Locate every Plasmodium parasite.
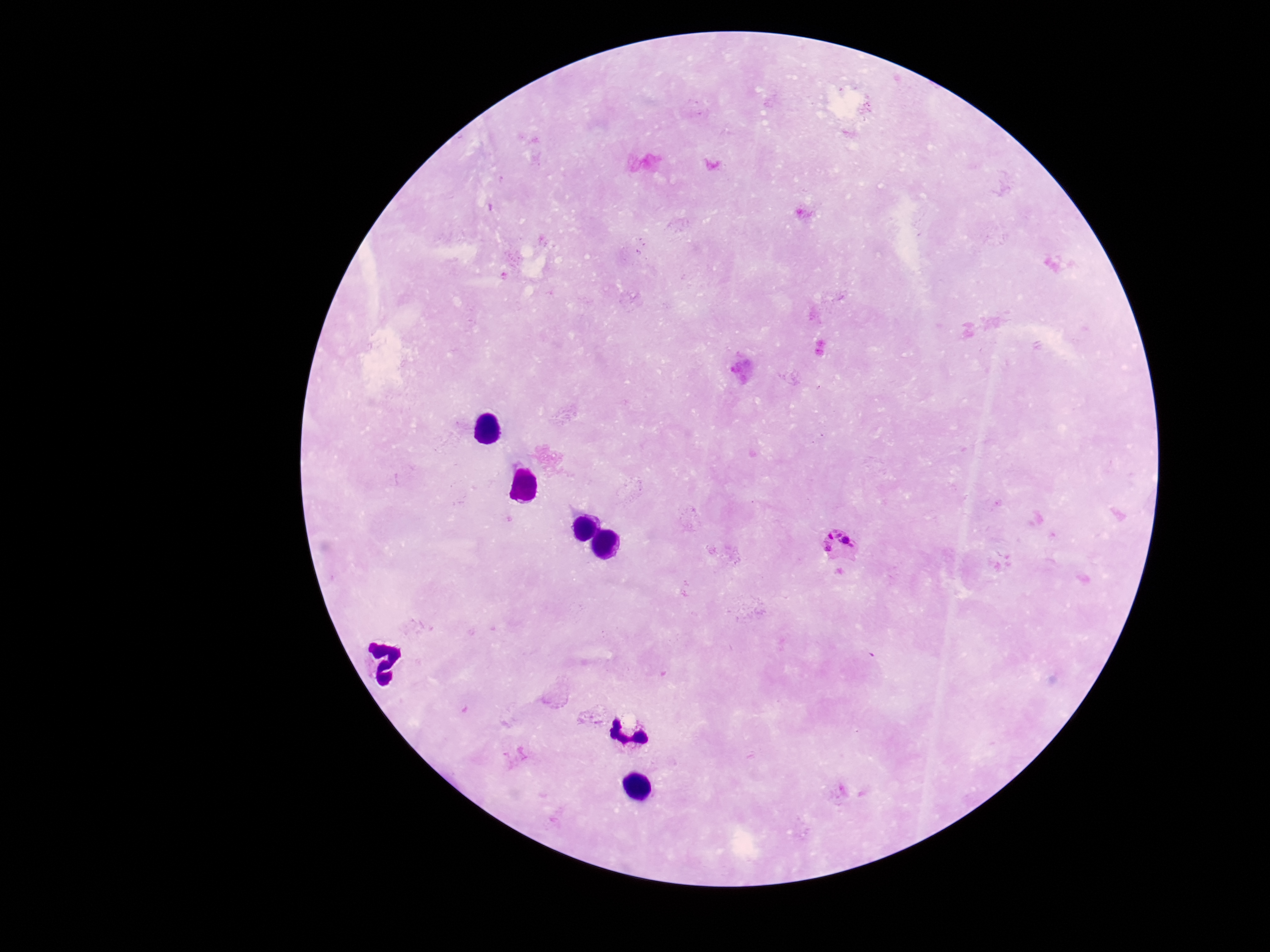

Approximate centers as (x, y) in pixels.
Plasmodium parasites: (841, 544).

image size = 1270×952 pixels
patient malaria status = positive
stain = Giemsa
magnification = 100x
capture = smartphone camera through the microscope eyepiece
field of view = one from this slide
preparation = thick blood film